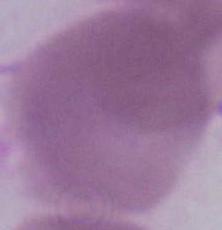 1000x magnification. An erythrocyte is shown. Photomicrograph.